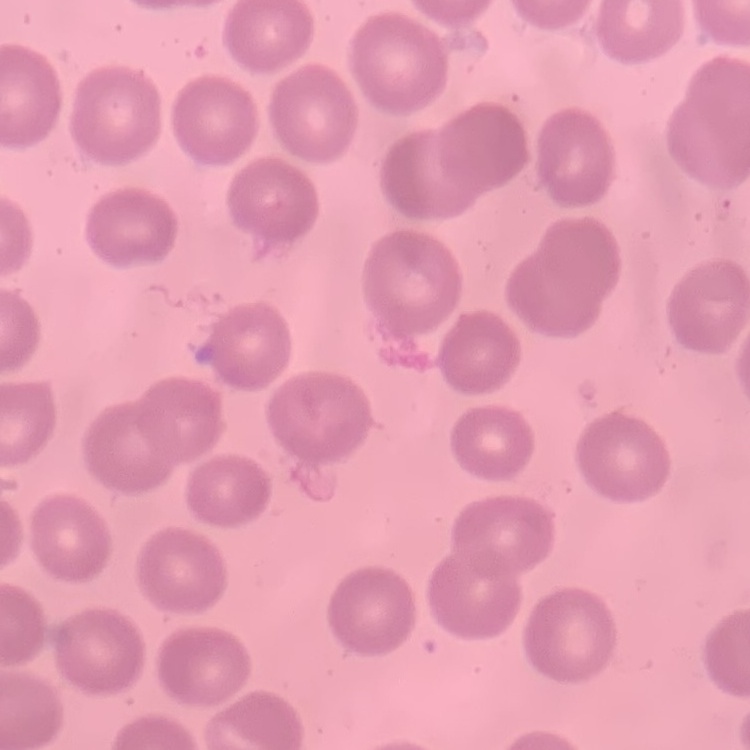
The erythrocytes show no rouleaux formation. One tile cut from a larger photomicrograph. Thin blood film. Stained with either Field's or Giemsa.